Report the malaria status of this cell.
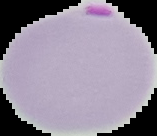
Parasitized.

Summary:
  - Preparation: thin blood film
  - Image type: cell region segmented out of the field of view; surrounding area masked to black
  - Image size: 157×136 pixels